Identify the blood parasite species.
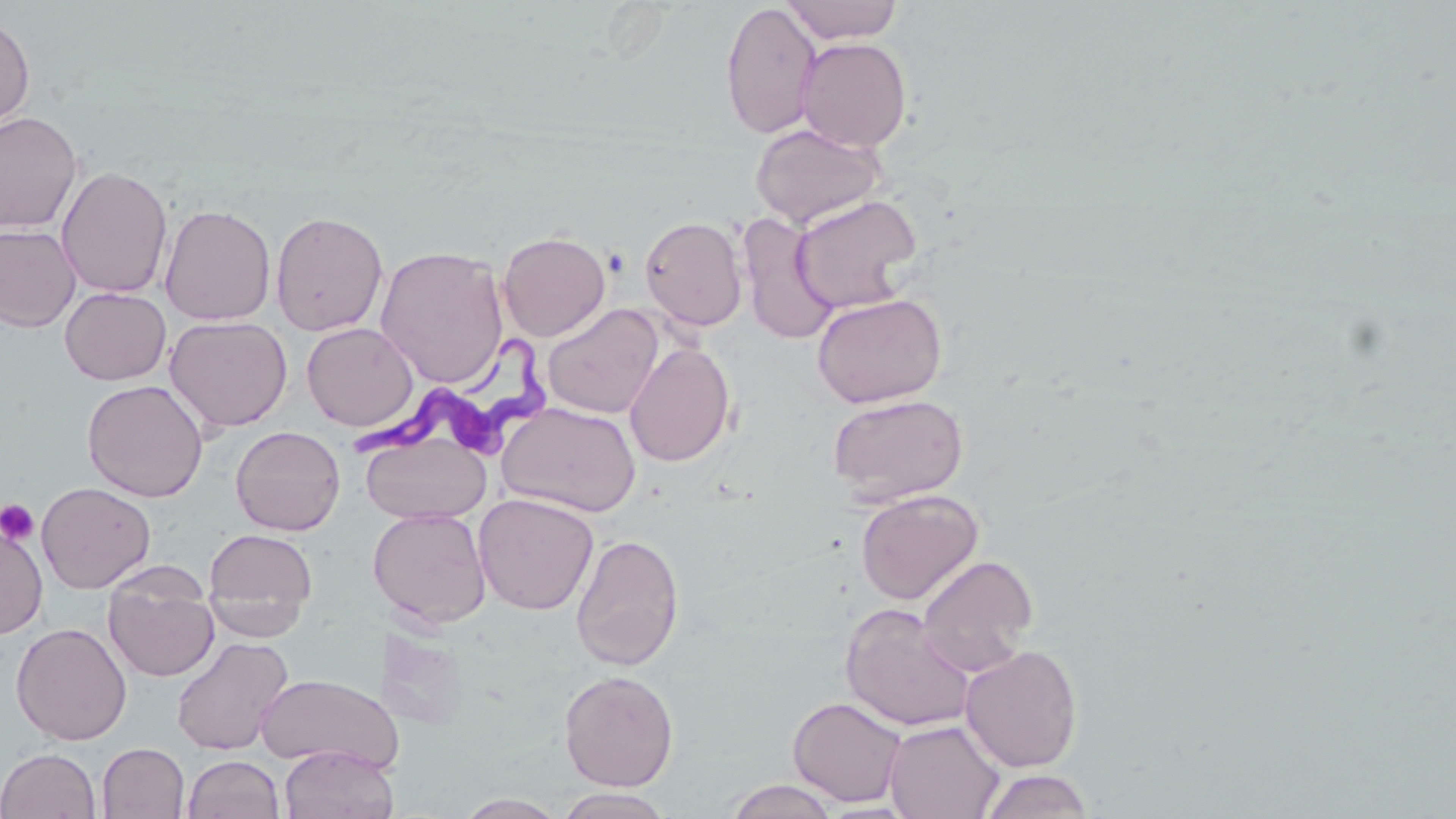
Trypanosoma brucei.

{
  "modality": "optical microscopy",
  "trypanosoma_brucei_locations": "approximate bounding boxes as (x1, y1, x2, y2) in pixels: (347, 326, 562, 481)",
  "platelet_locations": "approximate bounding boxes as (x1, y1, x2, y2) in pixels: (0, 499, 39, 545)",
  "preparation": "thin blood film",
  "image_size": "1456×819 pixels",
  "field_of_view": "single",
  "uninfected_red_blood_cell_locations": "approximate bounding boxes as (x1, y1, x2, y2) in pixels: (781, 0, 904, 44), (720, 1, 822, 140), (0, 14, 34, 130), (796, 37, 912, 152), (0, 110, 82, 234), (749, 123, 888, 229), (56, 166, 173, 298), (789, 193, 924, 314), (160, 204, 276, 326), (270, 210, 389, 336), (736, 214, 841, 344), (640, 215, 748, 331), (0, 224, 81, 332), (497, 231, 611, 341), (375, 245, 509, 388), (60, 287, 171, 385), (811, 292, 947, 408), (542, 303, 665, 419), (165, 316, 292, 432), (302, 323, 418, 431), (625, 342, 736, 467), (82, 379, 209, 502), (826, 392, 969, 505), (498, 402, 641, 518), (231, 425, 345, 535), (361, 432, 490, 524), (37, 481, 155, 593), (855, 489, 983, 605), (474, 493, 598, 615), (368, 508, 492, 629), (0, 524, 47, 638), (204, 527, 318, 635), (570, 533, 685, 671), (917, 553, 1039, 676), (103, 572, 219, 682), (840, 602, 976, 732), (11, 622, 131, 745), (170, 636, 293, 756), (960, 644, 1083, 771), (559, 669, 679, 791), (256, 673, 402, 772), (788, 695, 908, 806), (884, 719, 1004, 818), (97, 743, 189, 818), (279, 745, 398, 819), (0, 747, 101, 818), (182, 755, 284, 819), (977, 768, 1096, 818), (724, 779, 840, 819), (554, 788, 677, 818), (453, 793, 570, 819)",
  "stain": "May-Grünwald-Giemsa",
  "magnification": "1000x"
}